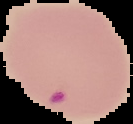
Summary:
  - Image size: 133×124 pixels
  - Malaria status: parasitized
  - Image type: segmented cell region on a black background
  - Preparation: thin blood smear